Describe the morphology of the red blood cells.
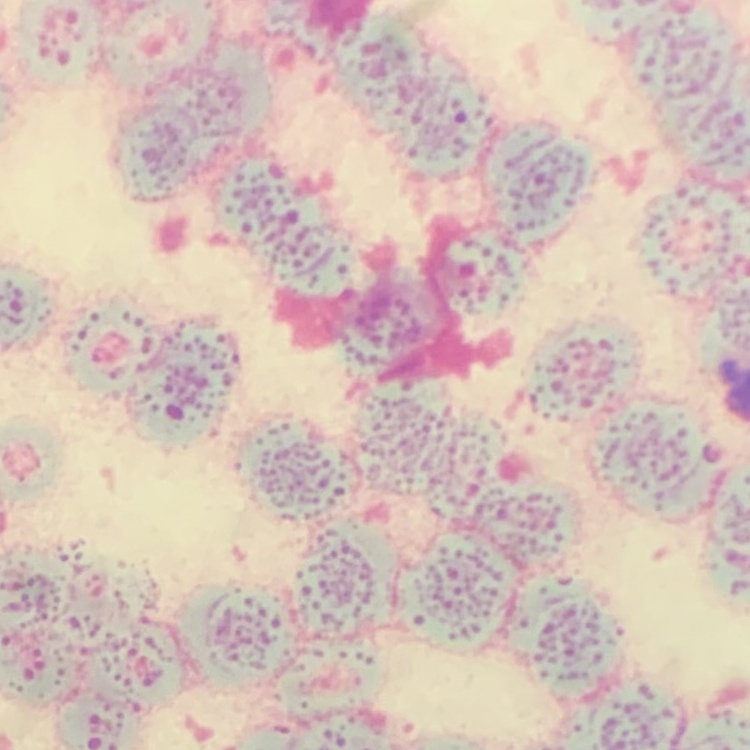

Rouleaux formation.

Summary:
  - Image type: one tile cut from a larger photomicrograph
  - Stain: Field's or Giemsa
  - Preparation: thin blood smear